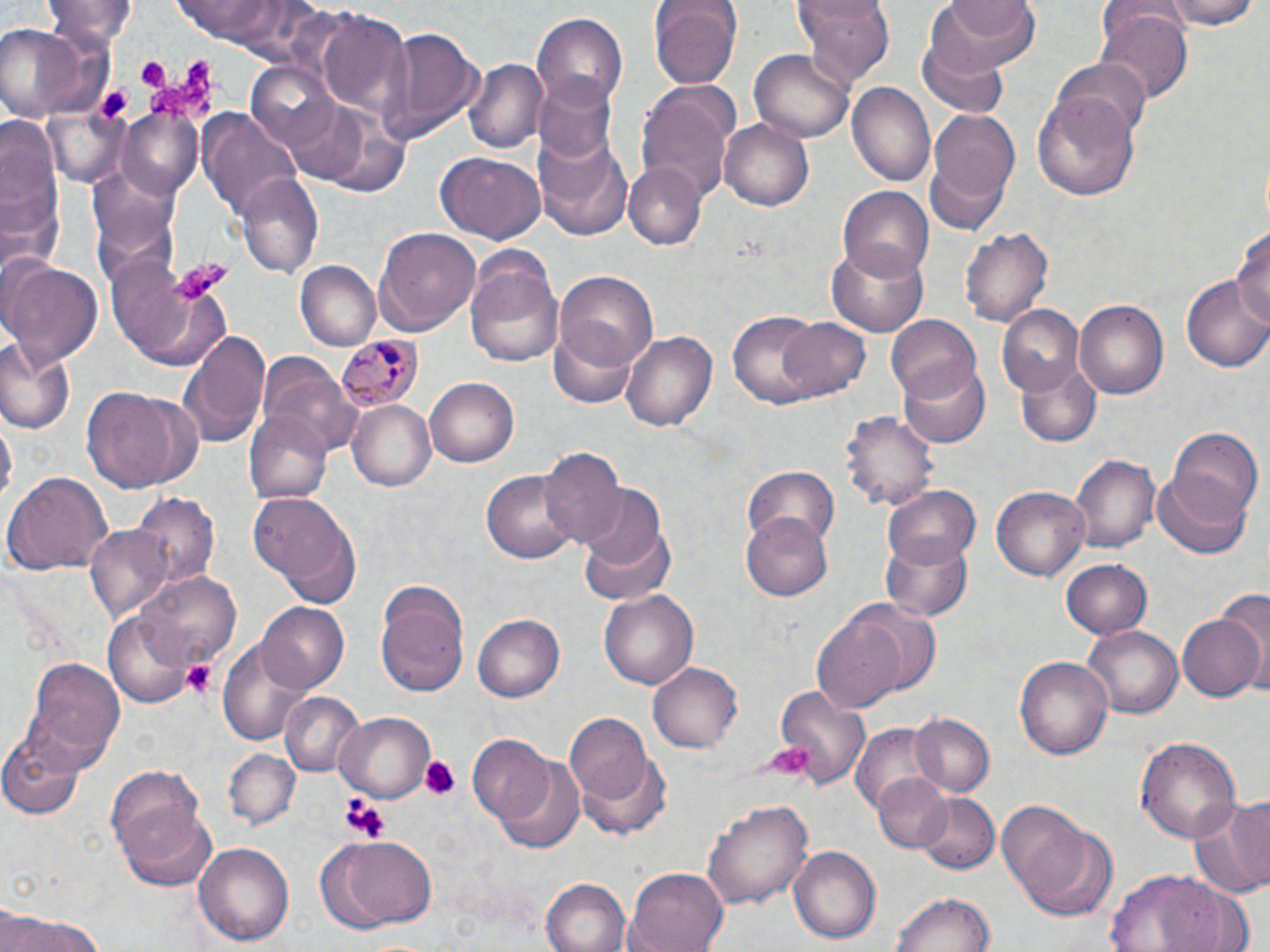

Summary:
  - Coordinate format: approximate bounding boxes as [x1, y1, x2, y2] in pixels
  - Plasmodium malariae-infected red blood cell locations: [336, 333, 424, 412]
  - Platelet locations: [132, 54, 172, 90], [144, 60, 220, 119], [175, 257, 229, 300], [181, 659, 219, 699], [768, 743, 817, 778], [419, 754, 462, 799], [338, 793, 389, 841]
  - Uninfected red blood cell locations: [164, 0, 329, 51], [646, 0, 744, 86], [792, 0, 897, 84], [926, 0, 1041, 71], [1167, 0, 1261, 28], [47, 1, 139, 50], [530, 10, 627, 112], [1095, 10, 1192, 103], [0, 22, 87, 123], [376, 28, 483, 142], [919, 35, 1010, 116], [749, 49, 854, 143], [1055, 57, 1151, 137], [463, 58, 547, 155], [244, 61, 344, 152], [535, 77, 616, 162], [849, 82, 934, 188], [637, 83, 739, 202], [1033, 88, 1143, 200], [926, 105, 1020, 214], [119, 108, 206, 196], [199, 110, 301, 220], [0, 115, 66, 278], [720, 116, 815, 213], [532, 124, 632, 239], [437, 151, 545, 243], [925, 155, 1011, 236], [625, 164, 705, 247], [234, 174, 322, 279], [837, 186, 934, 284], [1232, 222, 1270, 335], [960, 225, 1055, 329], [376, 226, 483, 334], [462, 243, 566, 367], [827, 244, 928, 336], [109, 252, 228, 366], [2, 259, 103, 367], [297, 263, 380, 352], [556, 270, 659, 371], [1182, 275, 1269, 372], [1074, 299, 1168, 399], [995, 301, 1085, 398], [729, 310, 842, 407], [886, 316, 980, 402], [776, 317, 872, 400], [551, 322, 640, 407], [178, 328, 270, 447], [621, 328, 718, 432], [0, 340, 75, 434], [260, 353, 359, 455], [1014, 360, 1100, 448], [899, 361, 991, 449], [424, 378, 520, 468], [80, 383, 203, 492], [348, 402, 435, 491], [247, 410, 332, 503], [841, 412, 938, 511], [1167, 427, 1261, 521], [538, 448, 626, 549], [1070, 454, 1159, 555], [743, 464, 839, 548], [1153, 469, 1253, 559], [4, 471, 113, 575], [482, 472, 577, 562], [882, 484, 980, 569], [993, 485, 1089, 582], [131, 491, 222, 582], [577, 491, 677, 605], [248, 492, 362, 607], [741, 510, 833, 599], [84, 523, 176, 623], [879, 533, 974, 622], [1059, 557, 1153, 639], [130, 571, 242, 670], [375, 583, 469, 701], [599, 589, 698, 689], [845, 599, 945, 698], [260, 603, 349, 693], [813, 611, 908, 714], [1176, 612, 1266, 702], [107, 613, 193, 706], [471, 614, 563, 703], [1083, 626, 1184, 719], [217, 635, 314, 749], [1016, 654, 1114, 761], [19, 655, 125, 771], [647, 662, 744, 754], [771, 684, 871, 788], [280, 693, 366, 780], [563, 710, 656, 812], [333, 712, 435, 802], [908, 713, 997, 798], [852, 722, 937, 814], [1, 730, 86, 819], [1135, 735, 1241, 845], [468, 737, 558, 831], [577, 748, 673, 841], [226, 749, 300, 829], [494, 755, 586, 853], [105, 764, 207, 868], [871, 774, 954, 855], [1186, 791, 1270, 900], [916, 792, 1000, 874], [703, 798, 814, 910], [117, 801, 217, 891], [996, 801, 1092, 903], [1021, 822, 1119, 920], [321, 835, 438, 928], [194, 841, 294, 946], [789, 847, 880, 944], [624, 866, 729, 952], [1105, 870, 1232, 952], [543, 878, 630, 952], [892, 890, 994, 952], [0, 913, 112, 952]
  - Slide-level diagnosis: Plasmodium malariae
  - Magnification: 1000x
  - Modality: light microscopy
  - Field of view: single
  - Image size: 1270×952 pixels
  - Preparation: thin blood smear
  - Stain: May-Grünwald-Giemsa